Report the malaria status of this cell.
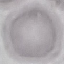

It is uninfected.

stain = Giemsa
capture = smartphone through the microscope eyepiece
image type = cell patch, automatically extracted from a larger field of view and resized to 64 × 64 pixels
preparation = thin smear